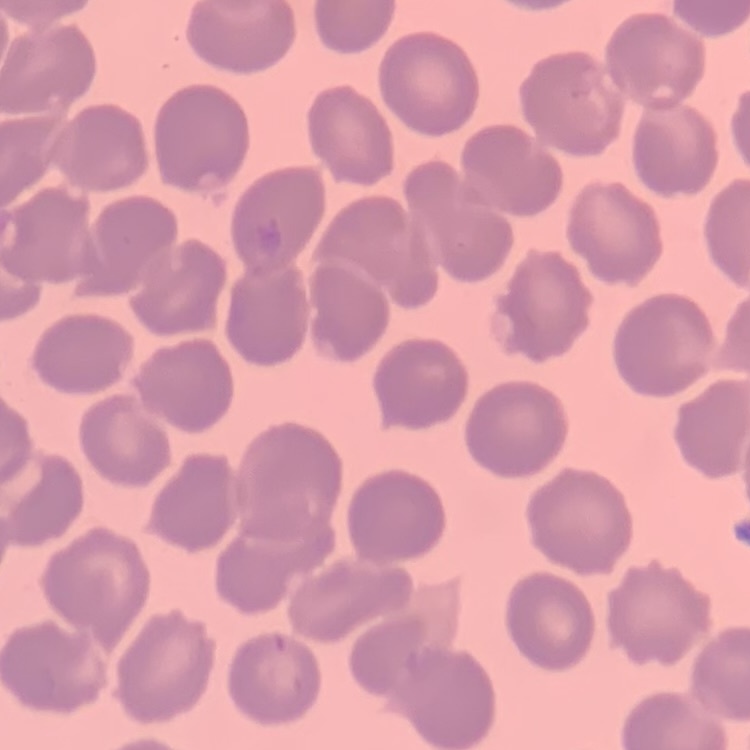
The red blood cells show no rouleaux formation. Square crop of a larger photomicrograph. Field's or Giemsa stain. Thin blood film.